Report the malaria status.
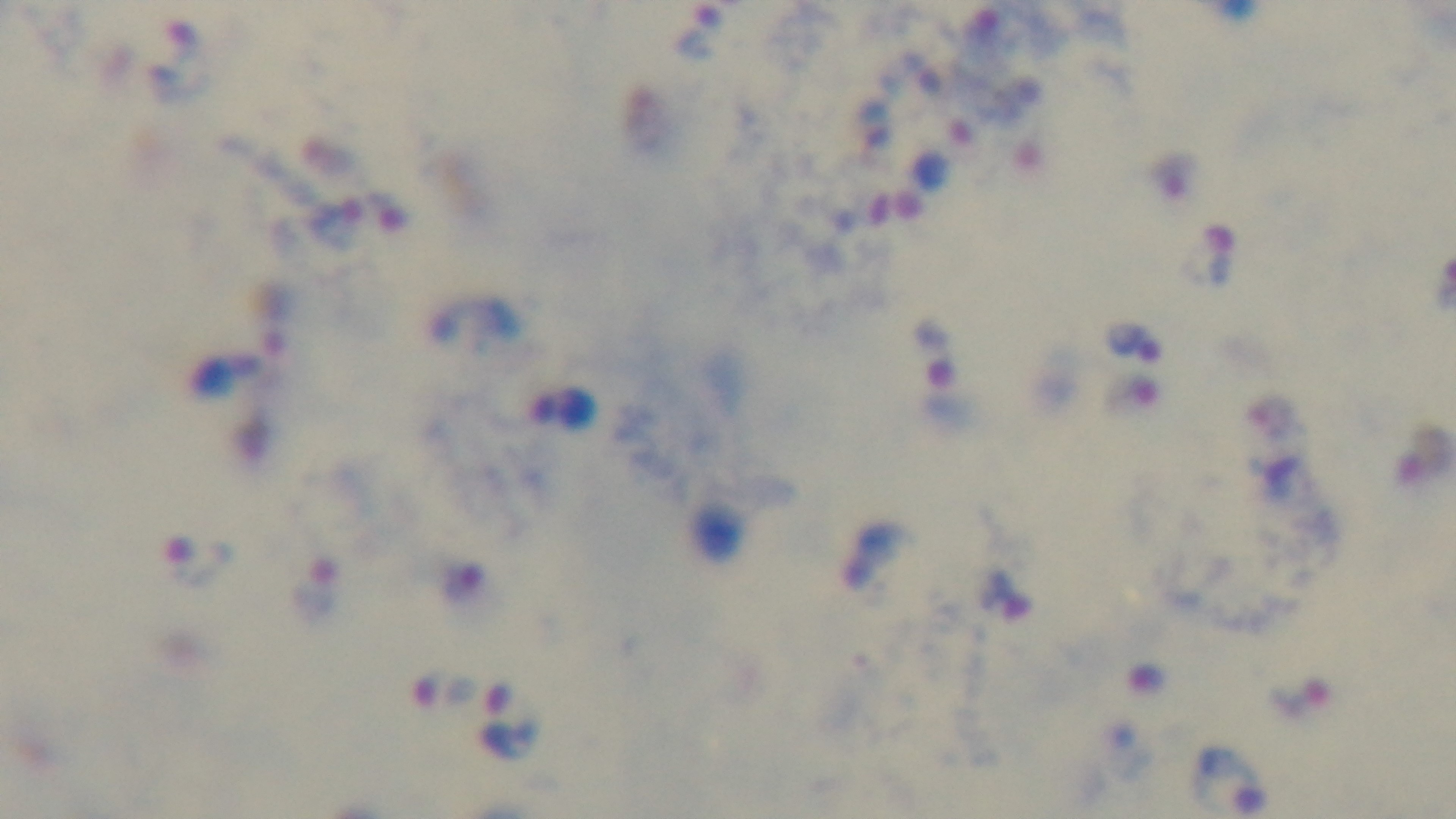
Infected.

Single field of view. Giemsa-stained. Preparation: thick blood film. 100x oil-immersion objective. Mounted 4K digital camera. Light microscopy.